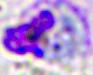 400x magnification. A white blood cell is seen. Photomicrograph.